Assess this cell for malaria.
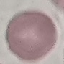
It is uninfected.

Thin blood smear. Photographed with a smartphone camera at the microscope eyepiece. Giemsa stain. Cell patch, automatically extracted from a larger field of view and resized to 64 × 64 pixels.